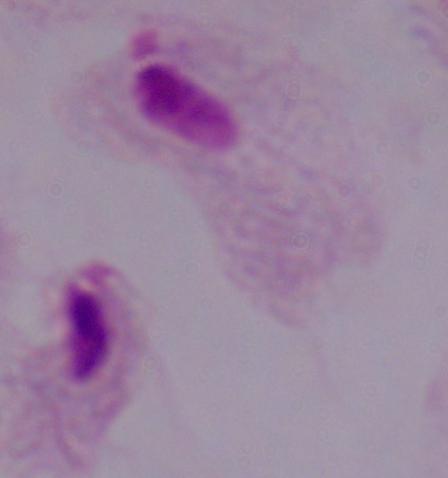
Summary:
  - Magnification: 1000x
  - Modality: micrograph
  - Identification: trichomonad